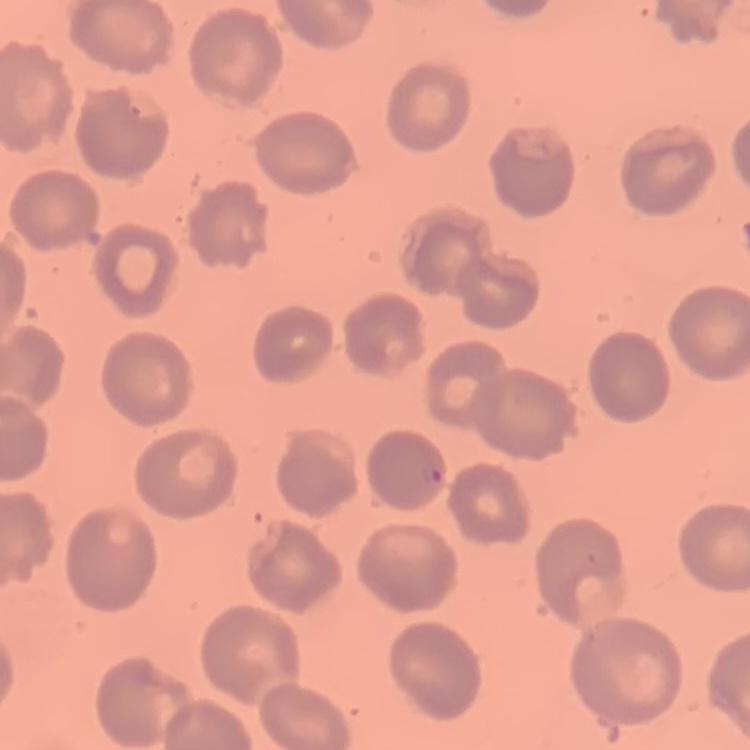
The red blood cells show no rouleaux formation. Thin blood smear. Square crop of a larger photomicrograph. Field's or Giemsa stain.